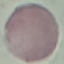

Summary:
  - Malaria status: uninfected
  - Stain: Giemsa
  - Capture: smartphone through the microscope eyepiece
  - Image type: cell patch, automatically extracted from a larger field of view and resized to 64 × 64 pixels
  - Preparation: thin blood film